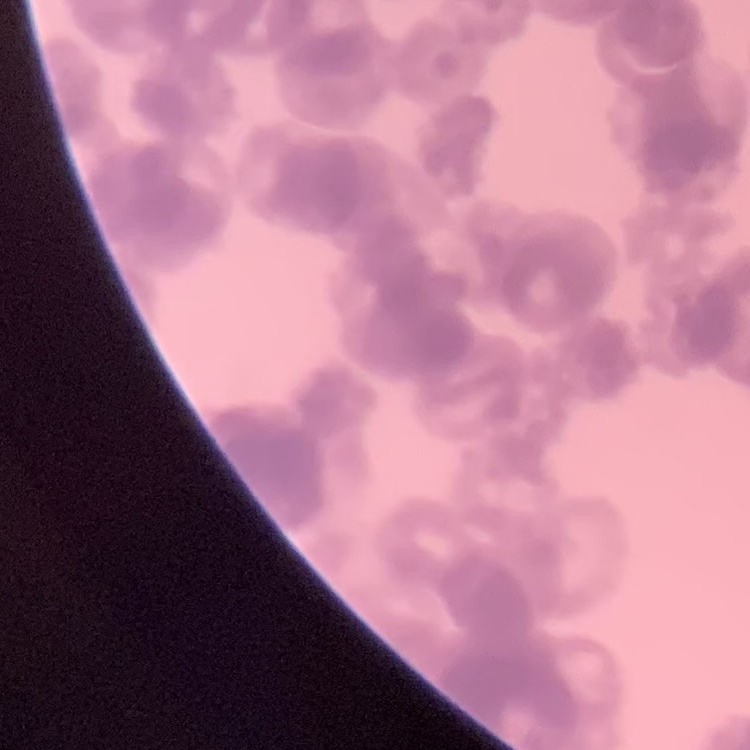

Summary:
  - Erythrocyte morphology: rouleaux formation
  - Image type: one tile cut from a larger photomicrograph
  - Preparation: thin blood film
  - Stain: Field's or Giemsa